Locate every Plasmodium falciparum-infected red blood cell.
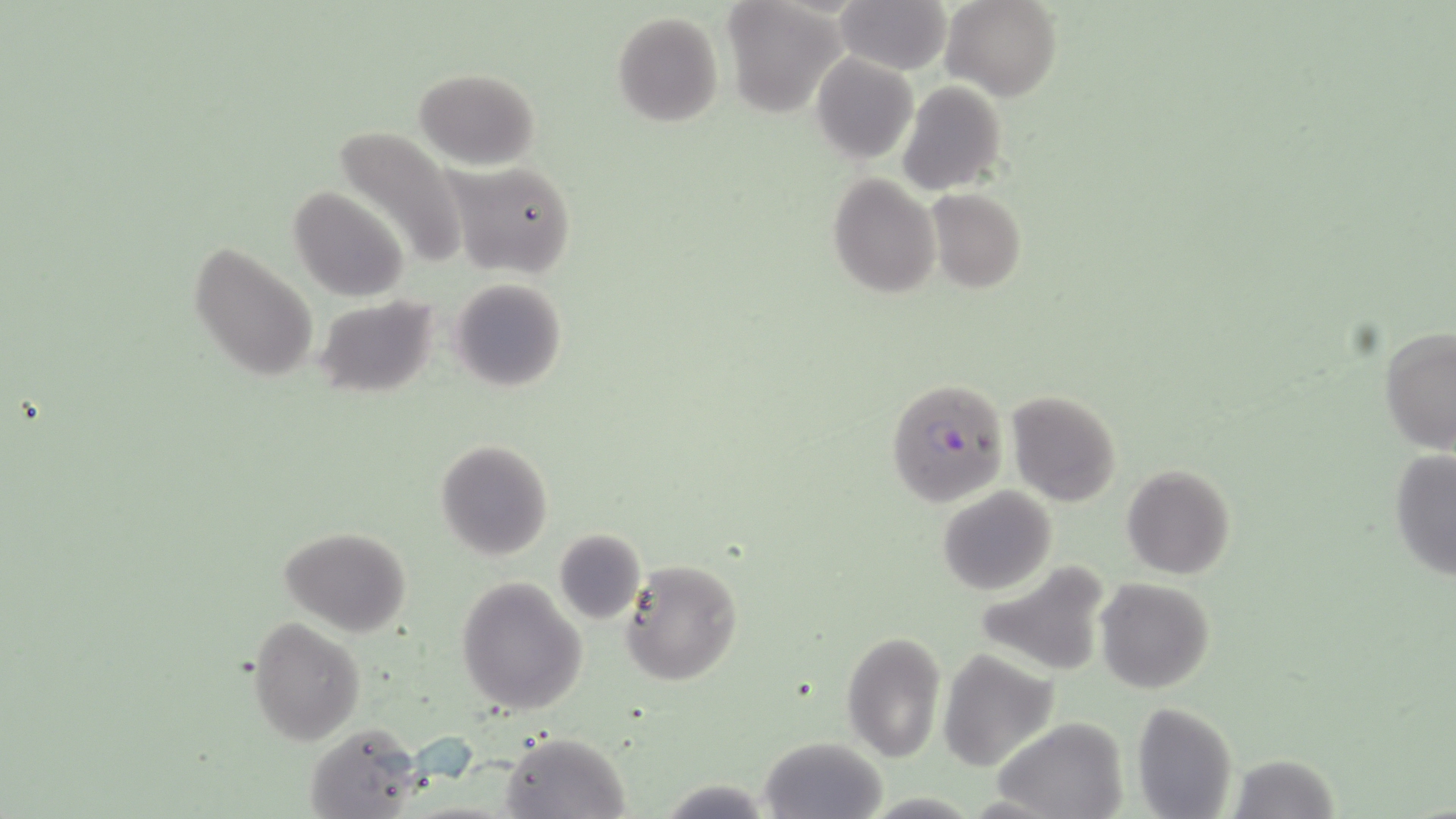
Approximate bounding boxes as (x1,y1)-(x2,y2) corner pairs in pixels.
Plasmodium falciparum-infected red blood cells: (886,378)-(1010,506).

Summary:
  - Uninfected red blood cell locations: (834,0)-(953,73), (942,0)-(1061,100), (722,2)-(844,116), (612,10)-(725,127), (810,52)-(918,164), (415,67)-(542,168), (898,81)-(1007,198), (330,126)-(469,272), (448,160)-(578,280), (827,174)-(939,298), (288,186)-(412,303), (926,188)-(1026,293), (187,241)-(320,384), (447,278)-(568,393), (314,295)-(442,401), (1380,326)-(1456,456), (1006,390)-(1124,508), (435,439)-(553,559), (1388,449)-(1456,583), (1121,464)-(1236,581), (937,487)-(1057,595), (280,526)-(410,638), (553,528)-(646,624), (618,558)-(743,686), (975,560)-(1111,676), (457,577)-(586,714), (1095,578)-(1214,693), (248,616)-(365,744), (841,632)-(945,762), (938,649)-(1057,771), (1133,701)-(1237,819), (991,715)-(1130,819), (302,724)-(426,818), (501,731)-(630,818), (759,736)-(886,818), (1226,755)-(1341,818), (657,778)-(774,817)
  - Slide-level diagnosis: Plasmodium falciparum
  - Image size: 1456×819 pixels
  - Magnification: 1000x
  - Field of view: single
  - Modality: optical microscopy
  - Preparation: thin blood smear
  - Stain: May-Grünwald-Giemsa